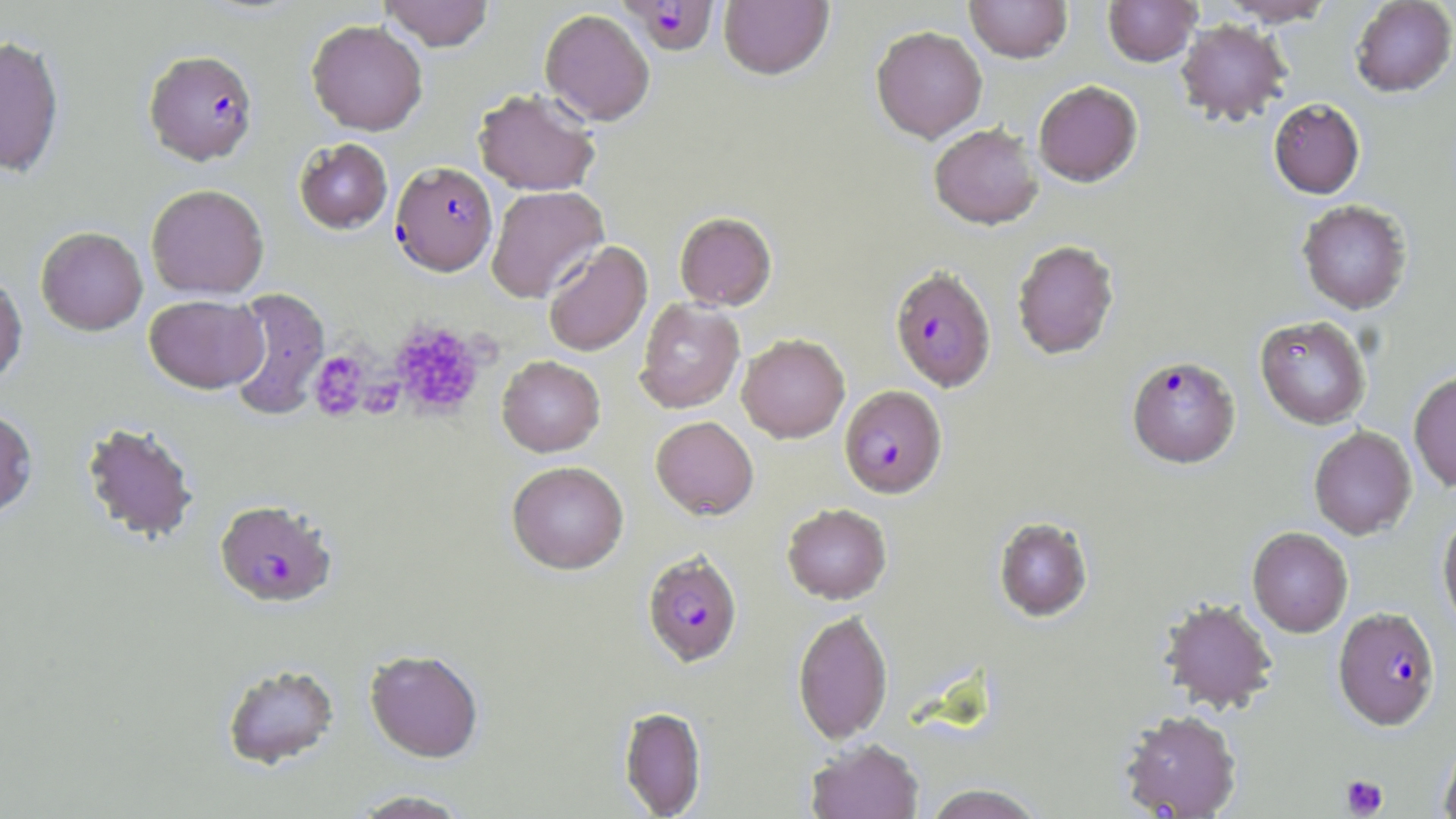

Summary:
  - Coordinate format: approximate bounding boxes as named x1/y1/x2/y2 corners in pixels
  - Uninfected red blood cell locations: (x1=379, y1=0, x2=495, y2=51), (x1=964, y1=0, x2=1072, y2=64), (x1=1103, y1=0, x2=1201, y2=67), (x1=1218, y1=0, x2=1337, y2=25), (x1=1350, y1=0, x2=1456, y2=97), (x1=719, y1=1, x2=834, y2=81), (x1=540, y1=9, x2=655, y2=126), (x1=306, y1=19, x2=428, y2=135), (x1=1175, y1=19, x2=1291, y2=126), (x1=871, y1=25, x2=987, y2=143), (x1=0, y1=34, x2=65, y2=177), (x1=1033, y1=80, x2=1143, y2=187), (x1=473, y1=87, x2=601, y2=195), (x1=1269, y1=98, x2=1365, y2=199), (x1=928, y1=123, x2=1044, y2=230), (x1=294, y1=138, x2=392, y2=234), (x1=146, y1=184, x2=269, y2=299), (x1=487, y1=185, x2=608, y2=303), (x1=1297, y1=200, x2=1412, y2=314), (x1=674, y1=211, x2=777, y2=310), (x1=36, y1=226, x2=148, y2=335), (x1=1011, y1=239, x2=1119, y2=360), (x1=543, y1=241, x2=652, y2=356), (x1=0, y1=272, x2=27, y2=386), (x1=225, y1=288, x2=330, y2=420), (x1=144, y1=294, x2=268, y2=393), (x1=635, y1=299, x2=745, y2=413), (x1=1255, y1=315, x2=1371, y2=429), (x1=737, y1=333, x2=850, y2=443), (x1=496, y1=355, x2=605, y2=457), (x1=1409, y1=371, x2=1456, y2=492), (x1=0, y1=408, x2=38, y2=520), (x1=650, y1=416, x2=759, y2=519), (x1=80, y1=421, x2=200, y2=544), (x1=1309, y1=426, x2=1417, y2=540), (x1=506, y1=461, x2=629, y2=574), (x1=781, y1=503, x2=892, y2=603), (x1=1438, y1=513, x2=1456, y2=634), (x1=994, y1=517, x2=1093, y2=622), (x1=1247, y1=526, x2=1353, y2=637), (x1=1159, y1=598, x2=1278, y2=714), (x1=792, y1=610, x2=893, y2=744), (x1=365, y1=649, x2=484, y2=763), (x1=220, y1=663, x2=340, y2=770), (x1=619, y1=705, x2=706, y2=817), (x1=1119, y1=709, x2=1242, y2=818), (x1=806, y1=739, x2=923, y2=819), (x1=1439, y1=739, x2=1456, y2=819), (x1=923, y1=784, x2=1046, y2=819), (x1=349, y1=789, x2=474, y2=818)
  - Platelet locations: (x1=389, y1=320, x2=487, y2=419), (x1=308, y1=350, x2=369, y2=421), (x1=358, y1=375, x2=405, y2=418), (x1=1340, y1=774, x2=1388, y2=817)
  - Plasmodium falciparum-infected red blood cell locations: (x1=618, y1=0, x2=720, y2=56), (x1=144, y1=49, x2=259, y2=165), (x1=390, y1=161, x2=497, y2=276), (x1=889, y1=264, x2=996, y2=392), (x1=1126, y1=355, x2=1241, y2=468), (x1=839, y1=385, x2=947, y2=498), (x1=214, y1=499, x2=338, y2=607), (x1=643, y1=551, x2=743, y2=667), (x1=1333, y1=607, x2=1441, y2=731)
  - Slide-level diagnosis: Plasmodium falciparum
  - Stain: May-Grünwald-Giemsa
  - Field of view: single
  - Preparation: thin blood film
  - Image size: 1456×819 pixels
  - Magnification: 1000x
  - Modality: optical microscopy